State which cell type is depicted.
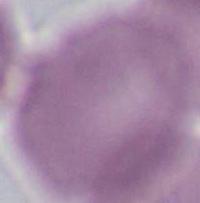

This is an erythrocyte.

Summary:
  - Magnification: 1000x
  - Modality: micrograph